Locate every uninfected red blood cell.
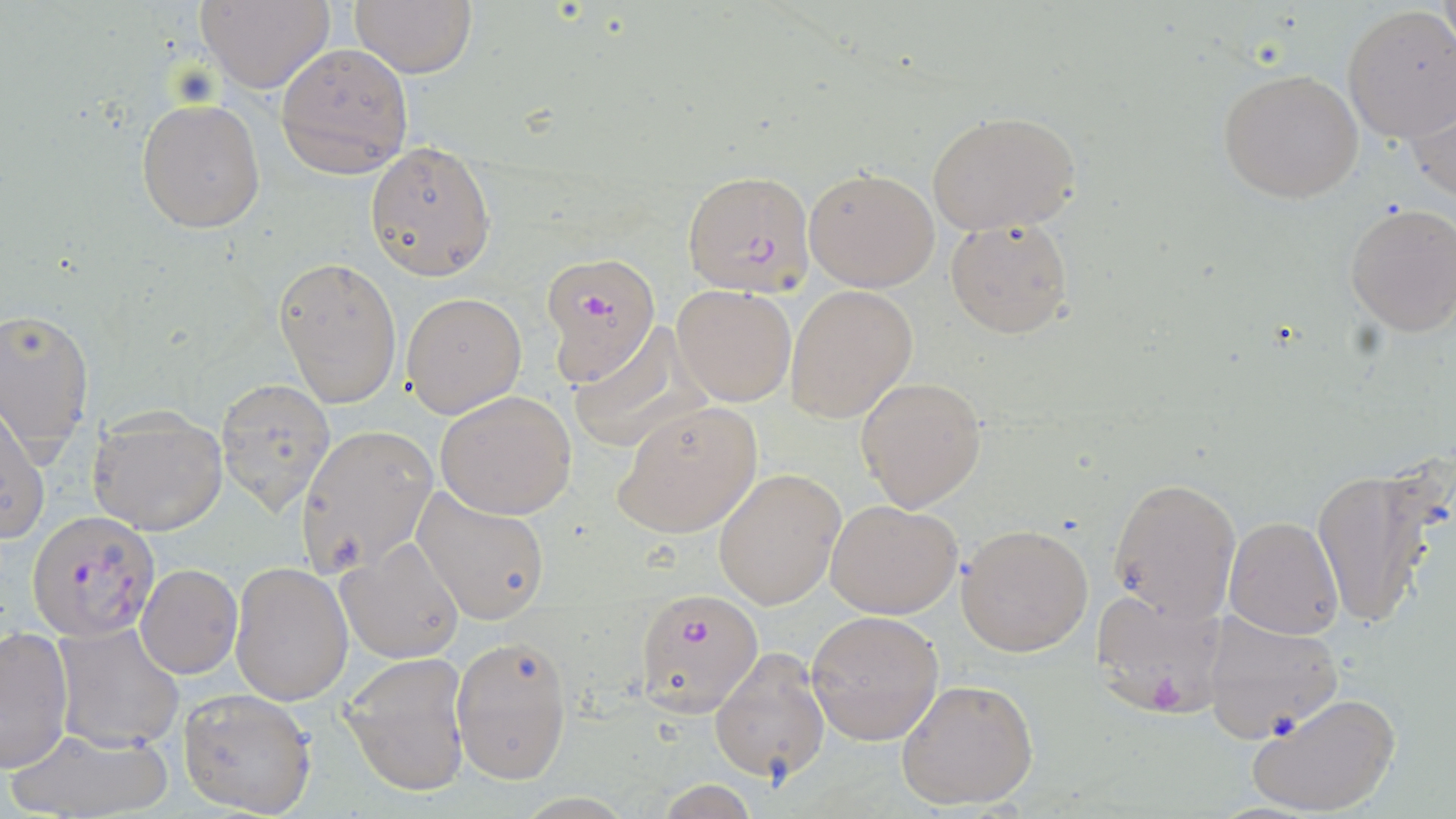

Approximate bounding boxes as named x1/y1/x2/y2 corners in pixels.
Uninfected red blood cells: (x1=195, y1=0, x2=336, y2=94), (x1=350, y1=1, x2=477, y2=78), (x1=1341, y1=5, x2=1456, y2=144), (x1=277, y1=42, x2=414, y2=176), (x1=1216, y1=68, x2=1363, y2=204), (x1=1409, y1=80, x2=1456, y2=209), (x1=137, y1=98, x2=266, y2=232), (x1=926, y1=109, x2=1082, y2=235), (x1=363, y1=139, x2=496, y2=280), (x1=803, y1=166, x2=941, y2=291), (x1=1343, y1=202, x2=1456, y2=338), (x1=944, y1=215, x2=1073, y2=339), (x1=273, y1=256, x2=401, y2=408), (x1=672, y1=284, x2=798, y2=407), (x1=785, y1=285, x2=917, y2=423), (x1=403, y1=291, x2=528, y2=417), (x1=0, y1=306, x2=96, y2=454), (x1=566, y1=322, x2=700, y2=454), (x1=855, y1=375, x2=987, y2=512), (x1=216, y1=378, x2=336, y2=515), (x1=435, y1=390, x2=579, y2=520), (x1=612, y1=401, x2=763, y2=540), (x1=0, y1=406, x2=50, y2=544), (x1=87, y1=412, x2=229, y2=536), (x1=294, y1=423, x2=438, y2=581), (x1=1312, y1=464, x2=1444, y2=631), (x1=714, y1=467, x2=845, y2=610), (x1=1107, y1=475, x2=1241, y2=623), (x1=410, y1=486, x2=552, y2=627), (x1=827, y1=499, x2=963, y2=619), (x1=1224, y1=516, x2=1343, y2=639), (x1=957, y1=521, x2=1094, y2=656), (x1=336, y1=537, x2=465, y2=663), (x1=228, y1=561, x2=353, y2=706), (x1=136, y1=563, x2=242, y2=678), (x1=89, y1=570, x2=214, y2=717), (x1=1200, y1=608, x2=1343, y2=744), (x1=806, y1=611, x2=944, y2=745), (x1=53, y1=623, x2=184, y2=750), (x1=1, y1=628, x2=73, y2=772), (x1=451, y1=632, x2=573, y2=785), (x1=709, y1=647, x2=830, y2=784), (x1=340, y1=650, x2=471, y2=797), (x1=895, y1=676, x2=1042, y2=811), (x1=176, y1=686, x2=317, y2=818), (x1=1244, y1=690, x2=1402, y2=818), (x1=7, y1=726, x2=174, y2=818).

Summary:
  - Plasmodium falciparum-infected red blood cell locations: (x1=683, y1=170, x2=815, y2=297), (x1=540, y1=250, x2=660, y2=383), (x1=28, y1=510, x2=157, y2=642), (x1=1092, y1=586, x2=1229, y2=720), (x1=634, y1=588, x2=764, y2=717)
  - Slide-level diagnosis: Plasmodium falciparum
  - Image size: 1456×819 pixels
  - Field of view: single
  - Stain: May-Grünwald-Giemsa
  - Modality: optical microscopy
  - Magnification: 1000x
  - Preparation: thin blood film